Mark where platelets are.
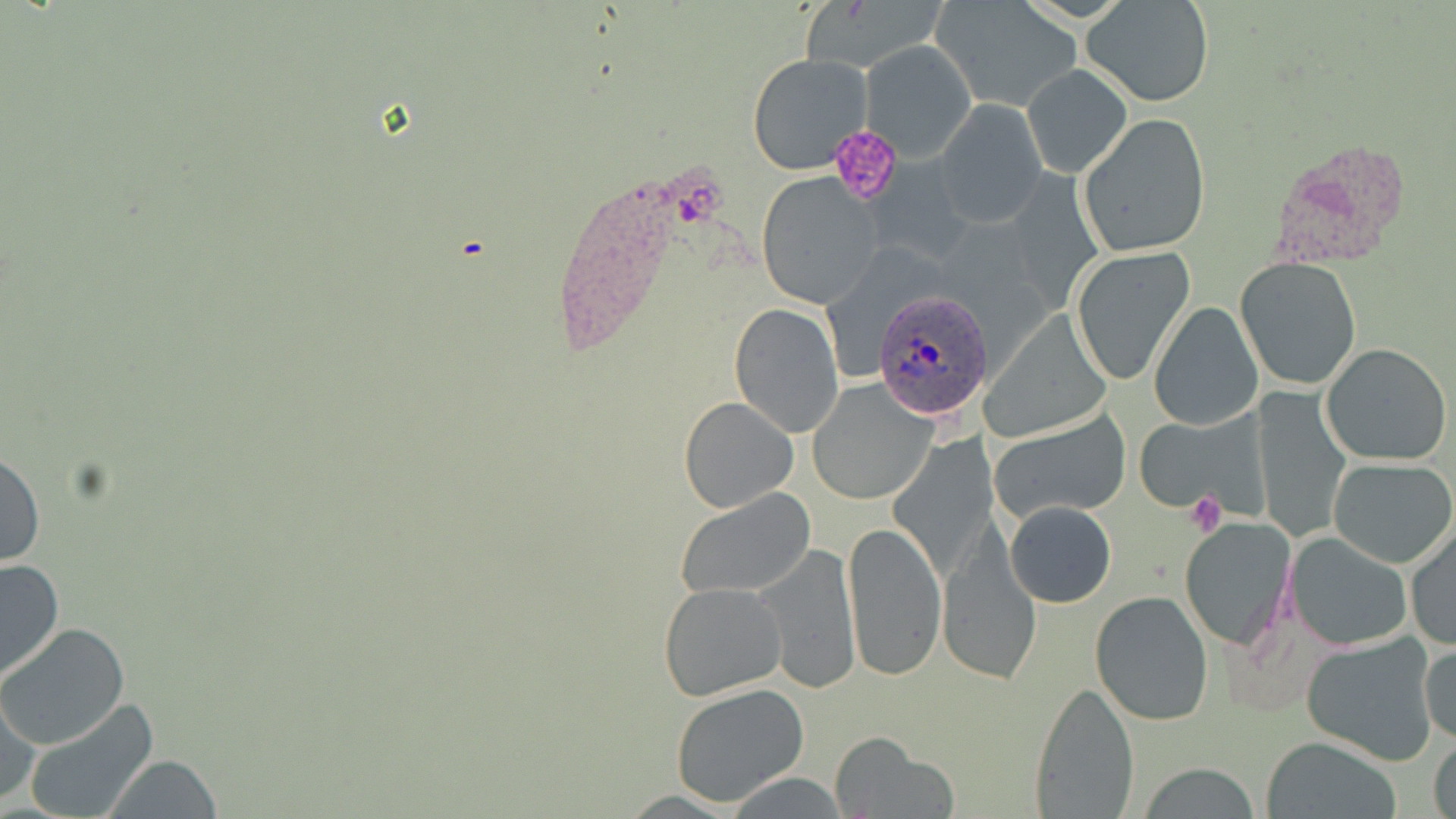
Approximate bounding boxes as (x1, y1, x2, y2) in pixels.
Platelets: (828, 123, 905, 203), (1186, 491, 1227, 537).

Plasmodium ovale-infected red blood cell locations = approximate bounding boxes as (x1, y1, x2, y2) in pixels: (876, 288, 990, 420)
slide-level diagnosis = Plasmodium ovale
field of view = one of a larger specimen
uninfected red blood cell locations = approximate bounding boxes as (x1, y1, x2, y2) in pixels: (1085, 0, 1213, 105), (934, 1, 1081, 111), (859, 38, 977, 161), (746, 53, 872, 173), (1023, 65, 1131, 177), (935, 100, 1045, 224), (1078, 113, 1211, 257), (754, 175, 881, 307), (1070, 245, 1195, 384), (1235, 256, 1364, 391), (1149, 301, 1264, 430), (729, 302, 844, 437), (979, 309, 1115, 443), (1320, 343, 1453, 466), (808, 381, 934, 505), (1251, 391, 1350, 542), (678, 395, 799, 512), (990, 409, 1132, 523), (1132, 413, 1260, 511), (888, 434, 995, 577), (1, 448, 44, 567), (1328, 457, 1456, 569), (675, 488, 815, 600), (1004, 500, 1117, 608), (842, 516, 947, 682), (1177, 517, 1298, 652), (1404, 522, 1455, 651), (1285, 531, 1411, 651), (938, 537, 1040, 686), (756, 543, 861, 692), (0, 558, 64, 683), (659, 583, 784, 700), (1090, 590, 1216, 727), (0, 624, 130, 750), (1301, 631, 1439, 763), (1420, 637, 1455, 747), (1028, 681, 1142, 818), (670, 684, 810, 806), (0, 691, 42, 807), (22, 700, 160, 819), (1430, 732, 1455, 819), (831, 734, 956, 818), (1263, 735, 1401, 818), (104, 754, 221, 819), (1136, 765, 1263, 818)
magnification = 1000x
image size = 1456×819 pixels
modality = light microscopy
stain = May-Grünwald-Giemsa
preparation = thin blood smear